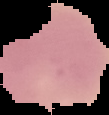
Image is 109×115 pixels. From a thin blood film. Malaria status: uninfected. The area outside the segmented cell region is set to black.